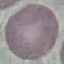
Summary:
  - Malaria status: uninfected
  - Preparation: thin blood smear
  - Image type: cell patch, automatically extracted from a larger field of view and resized to 64 × 64 pixels
  - Capture: smartphone camera at the microscope eyepiece
  - Stain: Giemsa